Report the malaria status of this cell.
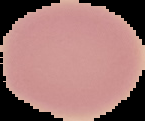
It is uninfected.

Summary:
  - Image type: segmented cell region on a black background
  - Preparation: thin blood smear
  - Image size: 145×121 pixels